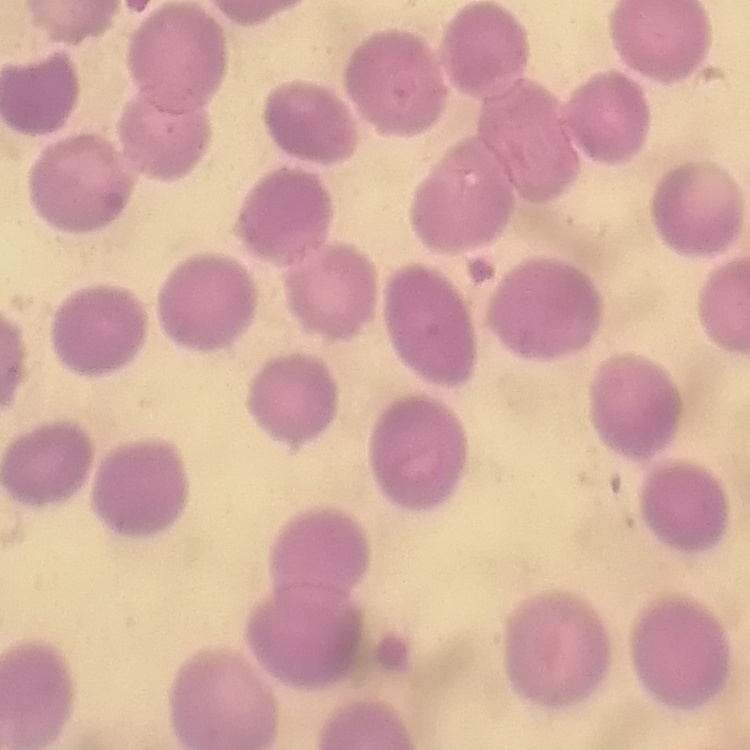

The erythrocytes exhibit no rouleaux formation. Square crop of a larger photomicrograph. Field's or Giemsa stain. Thin peripheral smear.